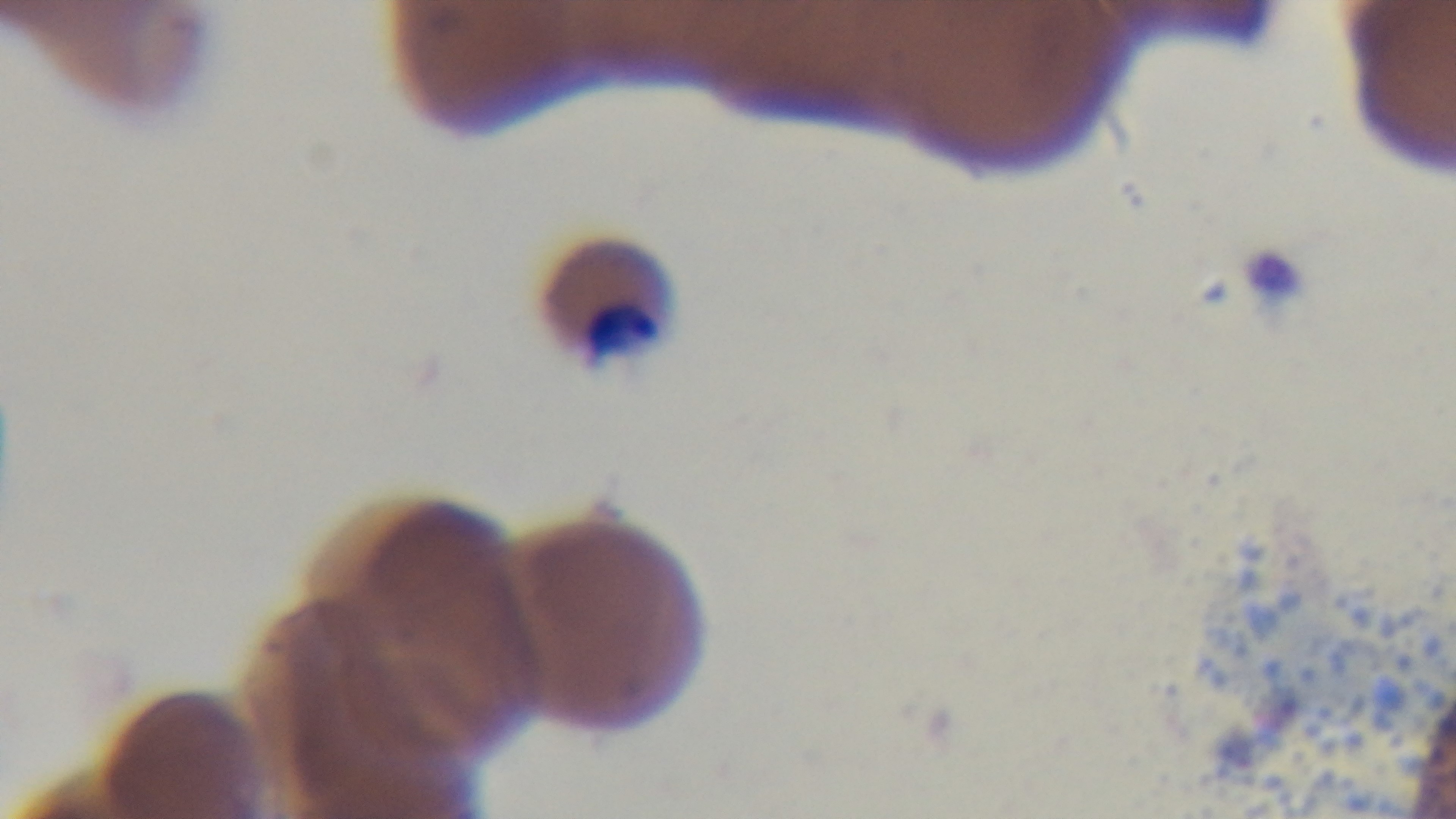 Photomicrograph. Preparation: thin smear. Mounted 4K digital camera. Giemsa stain. 100x oil-immersion objective. Malaria status: infected. Single field of view.